Report the malaria status of this cell.
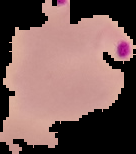
Parasitized.

image size = 136×154 pixels
image type = segmented cell region with the area outside set to black
preparation = thin blood film